Describe the morphology of the erythrocytes.
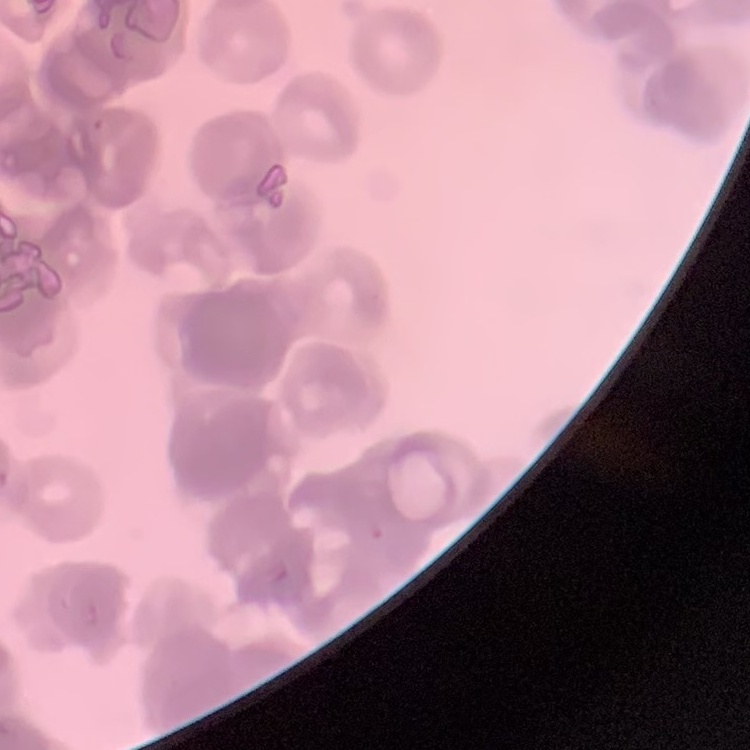

Rouleaux formation.

Stained with either Field's or Giemsa. Thin blood film. Square crop of a larger photomicrograph.